Outline each Plasmodium falciparum-infected red blood cell.
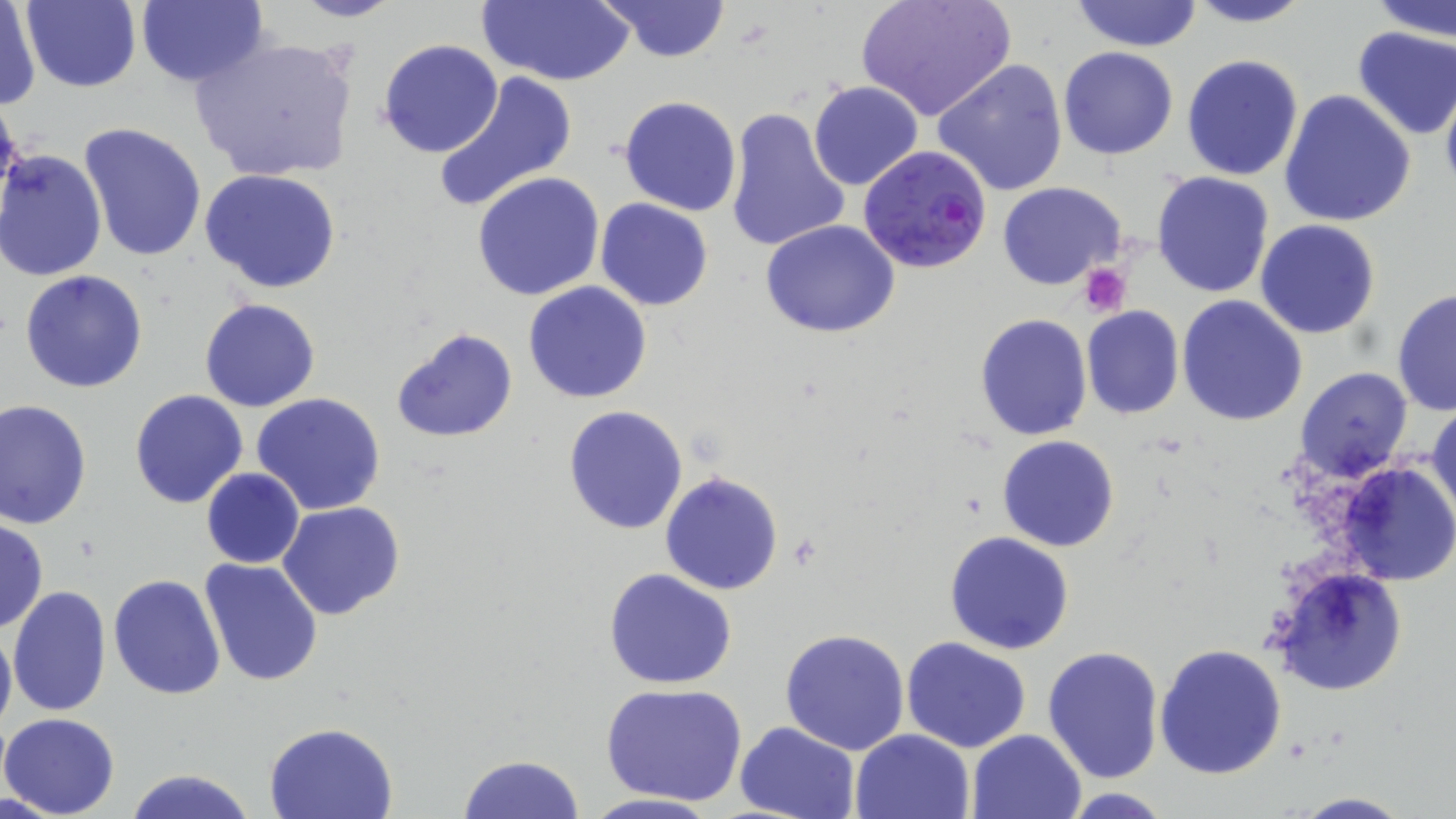

Approximate bounding boxes as [x1, y1, x2, y2] in pixels.
Plasmodium falciparum-infected red blood cells: [860, 147, 993, 274].

Summary:
  - Platelet locations: [1078, 263, 1131, 317]
  - Uninfected red blood cell locations: [23, 0, 142, 92], [277, 0, 404, 23], [478, 0, 633, 87], [596, 0, 732, 63], [856, 0, 1014, 122], [1070, 0, 1203, 51], [1183, 0, 1315, 27], [1370, 0, 1456, 41], [136, 1, 267, 89], [1, 3, 40, 111], [1352, 26, 1456, 139], [190, 34, 360, 185], [377, 39, 504, 157], [1059, 46, 1180, 160], [1180, 54, 1304, 182], [931, 57, 1069, 197], [433, 69, 579, 212], [1439, 80, 1456, 198], [808, 81, 924, 191], [1279, 89, 1417, 229], [619, 95, 742, 217], [0, 96, 25, 216], [723, 106, 852, 253], [78, 123, 208, 265], [0, 149, 108, 282], [200, 167, 342, 294], [1152, 171, 1275, 298], [471, 172, 606, 301], [997, 181, 1126, 290], [595, 199, 713, 312], [759, 219, 902, 338], [1255, 219, 1381, 338], [20, 270, 148, 393], [523, 281, 653, 404], [1390, 285, 1456, 418], [1177, 296, 1308, 426], [199, 298, 321, 412], [1081, 306, 1185, 418], [975, 313, 1093, 440], [390, 327, 517, 445], [1295, 366, 1414, 481], [130, 390, 249, 510], [252, 392, 386, 515], [1, 398, 94, 529], [1428, 398, 1456, 527], [562, 406, 688, 534], [996, 435, 1120, 552], [1336, 461, 1456, 586], [201, 469, 306, 565], [661, 472, 784, 594], [278, 501, 404, 619], [0, 518, 48, 633], [943, 531, 1075, 655], [201, 560, 324, 686], [1271, 566, 1408, 697], [603, 568, 737, 689], [108, 573, 227, 700], [8, 585, 112, 717], [0, 620, 16, 740], [780, 628, 910, 754], [902, 636, 1033, 753], [1155, 642, 1287, 778], [1041, 644, 1164, 783], [599, 682, 748, 806], [1, 711, 121, 819], [733, 719, 859, 819], [265, 721, 400, 819], [850, 729, 974, 819], [969, 729, 1089, 819], [458, 754, 586, 818], [124, 766, 258, 819], [1060, 788, 1178, 819], [578, 792, 721, 819], [1287, 792, 1418, 818]
  - Slide-level diagnosis: Plasmodium falciparum
  - Preparation: thin blood smear
  - Stain: May-Grünwald-Giemsa
  - Modality: optical microscopy
  - Image size: 1456×819 pixels
  - Magnification: 1000x
  - Field of view: one of a larger specimen